Describe the morphology of the erythrocytes.
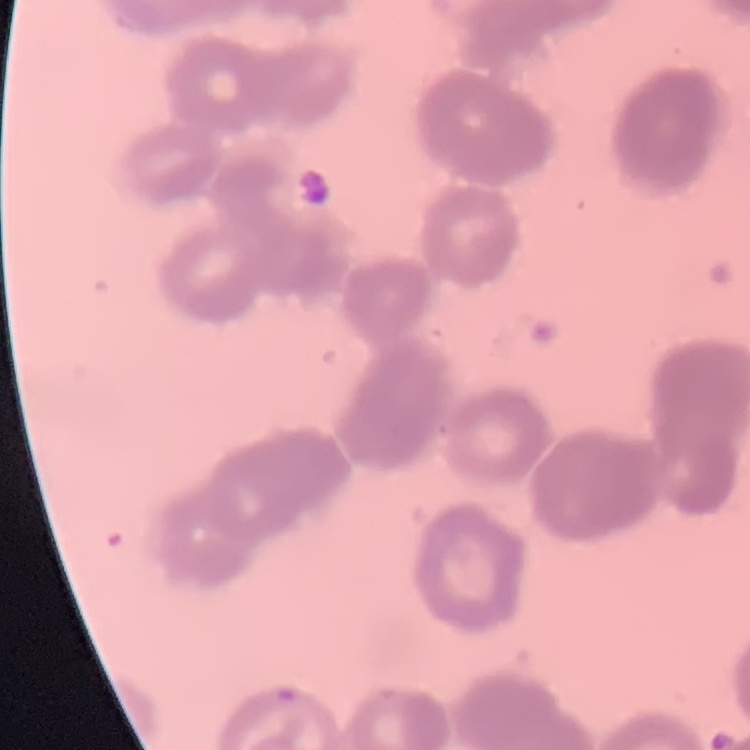

Rouleaux formation.

stain = Field's or Giemsa
preparation = thin peripheral smear
image type = square crop of a larger photomicrograph